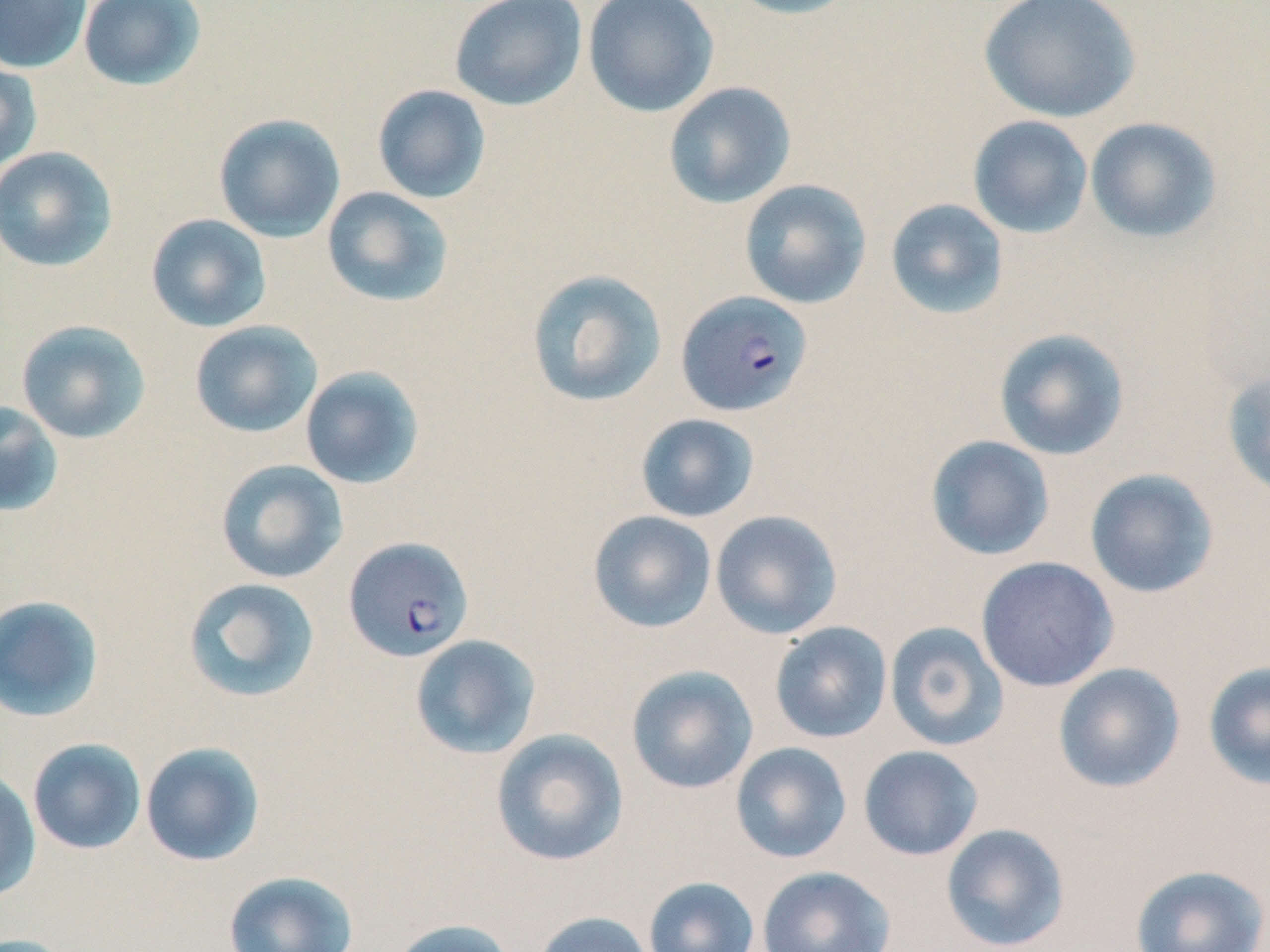
Summary:
  - Coordinate format: approximate bounding boxes as [x1, y1, x2, y2] in pixels
  - Uninfected red blood cell locations: [0, 0, 91, 74], [77, 0, 206, 91], [449, 0, 588, 111], [583, 0, 719, 118], [723, 0, 860, 19], [978, 0, 1141, 123], [0, 57, 43, 174], [663, 82, 796, 209], [371, 84, 491, 204], [213, 113, 346, 242], [967, 115, 1093, 239], [1084, 117, 1222, 244], [0, 146, 118, 272], [739, 179, 872, 309], [321, 186, 454, 308], [885, 198, 1010, 319], [145, 213, 272, 333], [525, 269, 668, 408], [16, 319, 151, 443], [189, 320, 323, 438], [993, 328, 1130, 461], [300, 366, 425, 490], [1221, 367, 1270, 500], [0, 401, 64, 518], [635, 413, 760, 523], [924, 435, 1054, 561], [215, 459, 348, 584], [1084, 468, 1220, 599], [588, 510, 717, 633], [710, 510, 843, 640], [975, 556, 1119, 692], [182, 576, 320, 703], [0, 595, 104, 722], [769, 621, 893, 743], [884, 621, 1009, 751], [410, 634, 541, 760], [1203, 661, 1270, 791], [1053, 663, 1186, 793], [626, 665, 759, 794], [490, 728, 629, 867], [27, 738, 147, 855], [139, 741, 265, 867], [730, 742, 853, 863], [858, 745, 984, 861], [0, 768, 41, 902], [940, 823, 1071, 952], [1129, 864, 1269, 952], [757, 865, 895, 952], [223, 870, 359, 952], [643, 876, 760, 952], [532, 911, 655, 952], [386, 918, 519, 952], [0, 933, 80, 952]
  - Plasmodium falciparum-infected red blood cell locations: [676, 290, 813, 417], [343, 536, 474, 663]
  - Slide-level diagnosis: Plasmodium falciparum
  - Image size: 1270×952 pixels
  - Stain: May-Grünwald-Giemsa
  - Modality: light microscopy
  - Preparation: thin blood film
  - Magnification: 1000x
  - Field of view: single